State which parasite is depicted.
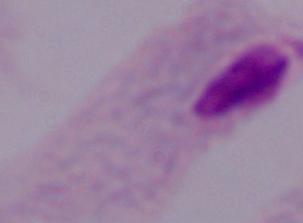

A trichomonad.

Summary:
  - Magnification: 1000x
  - Modality: photomicrograph